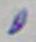
magnification = 1000x
identification = Toxoplasma gondii
modality = photomicrograph